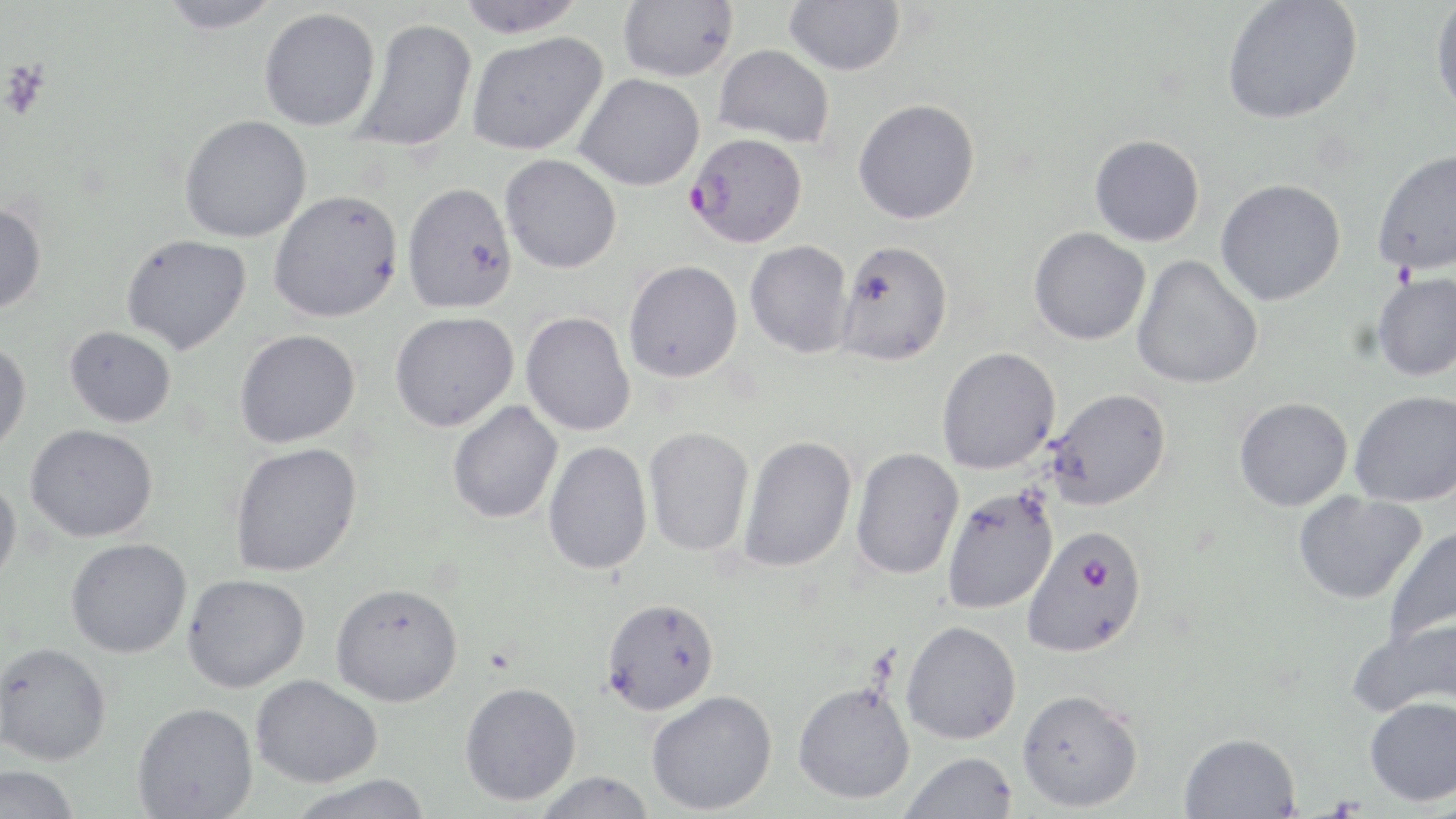

slide-level diagnosis = Plasmodium falciparum
stain = May-Grünwald-Giemsa
platelet locations = approximate bounding boxes as (x1, y1, x2, y2) in pixels: (1, 61, 51, 119)
preparation = thin blood smear
magnification = 1000x
modality = light microscopy
field of view = single
Plasmodium falciparum-infected red blood cell locations = approximate bounding boxes as (x1, y1, x2, y2) in pixels: (686, 133, 807, 248), (1021, 524, 1148, 658)
image size = 1456×819 pixels
uninfected red blood cell locations = approximate bounding boxes as (x1, y1, x2, y2) in pixels: (157, 0, 283, 34), (456, 0, 587, 38), (618, 0, 738, 82), (784, 0, 905, 76), (1222, 0, 1363, 124), (1430, 1, 1456, 122), (259, 7, 380, 131), (353, 18, 478, 152), (466, 31, 608, 156), (714, 44, 835, 148), (573, 73, 705, 191), (853, 99, 980, 224), (179, 114, 312, 243), (1089, 134, 1205, 246), (1371, 147, 1456, 276), (500, 154, 622, 273), (1216, 178, 1346, 305), (402, 181, 518, 314), (268, 189, 404, 323), (0, 202, 46, 314), (1029, 227, 1151, 345), (120, 233, 252, 354), (834, 239, 953, 366), (745, 240, 854, 358), (1132, 255, 1263, 390), (623, 260, 743, 382), (1371, 271, 1456, 382), (521, 311, 635, 436), (390, 312, 519, 432), (65, 325, 177, 427), (235, 329, 361, 448), (0, 341, 31, 456), (936, 346, 1061, 475), (1046, 387, 1171, 511), (1350, 390, 1456, 507), (1234, 397, 1352, 511), (447, 400, 563, 524), (26, 423, 158, 542), (643, 426, 754, 557), (738, 434, 857, 573), (229, 441, 362, 577), (543, 441, 652, 574), (851, 447, 964, 579), (0, 474, 22, 586), (941, 486, 1059, 614), (1293, 491, 1426, 604), (1382, 525, 1456, 647), (65, 537, 192, 658), (182, 574, 311, 692), (331, 582, 463, 707), (601, 597, 719, 715), (1348, 615, 1456, 721), (901, 620, 1021, 744), (0, 642, 111, 765), (251, 674, 383, 787), (459, 681, 582, 806), (792, 682, 915, 805), (1017, 688, 1143, 812), (646, 690, 777, 815), (1365, 696, 1456, 806), (132, 702, 258, 819), (1179, 732, 1301, 819), (900, 751, 1018, 818), (0, 765, 80, 819), (533, 771, 658, 818), (286, 775, 434, 819)